Report the malaria status of this cell.
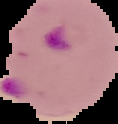
It is parasitized.

image type = segmented cell region on a black background
preparation = thin blood smear
image size = 118×124 pixels